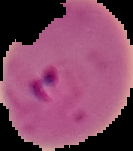
result = Plasmodium parasites detected
image size = 133×151 pixels
preparation = thin blood smear
image type = cell region segmented out of the field of view; surrounding area masked to black